State the preparation type.
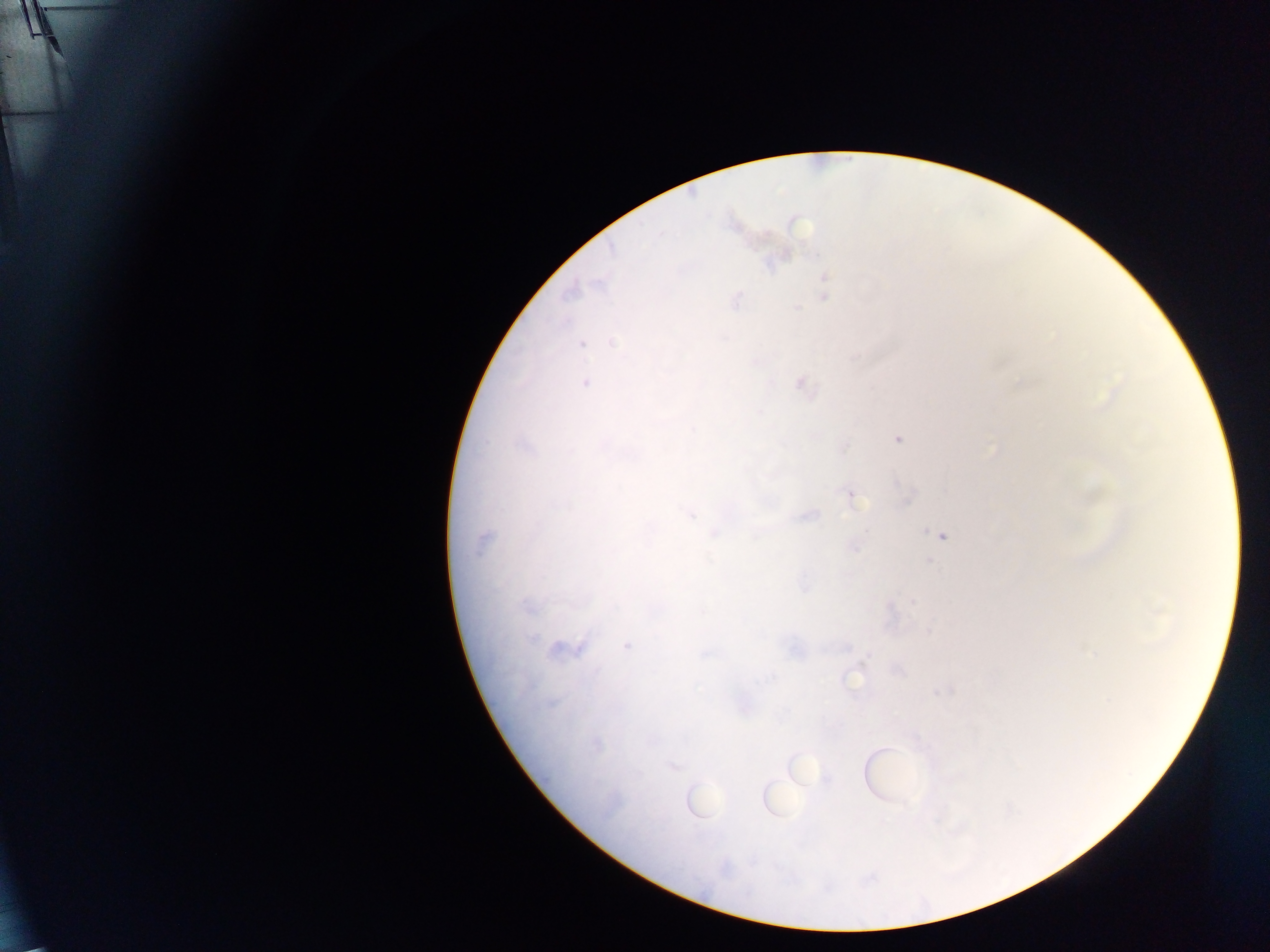

This is a thick smear.

malaria parasite locations = approximate centers as (x, y) in pixels: (6, 56), (824, 277), (823, 297), (735, 299), (796, 308), (612, 342), (581, 344), (585, 383), (801, 383), (897, 438), (603, 445), (844, 448), (897, 484), (851, 495), (908, 499), (689, 514), (808, 515), (713, 533), (941, 535), (482, 541), (854, 548), (928, 561), (804, 587), (912, 601), (527, 608), (1157, 611), (929, 630), (626, 646), (845, 647), (558, 649), (578, 649), (1093, 653), (899, 671), (851, 681), (552, 703), (597, 745), (673, 766), (827, 780)
capture = mobile-phone photograph through a microscope
field of view = single
country = Ghana
image size = 1270×952 pixels